Identify the parasite.
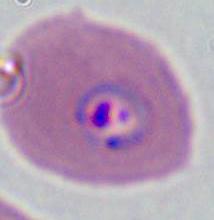

This is Plasmodium.

Micrograph. Captured at either 400x or 1000x magnification.